Assess this cell for malaria.
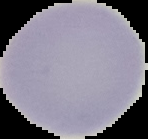
Uninfected.

Cell region segmented out of the field of view; the surrounding area is masked to black. From a thin blood film. Image is 148×139 pixels.